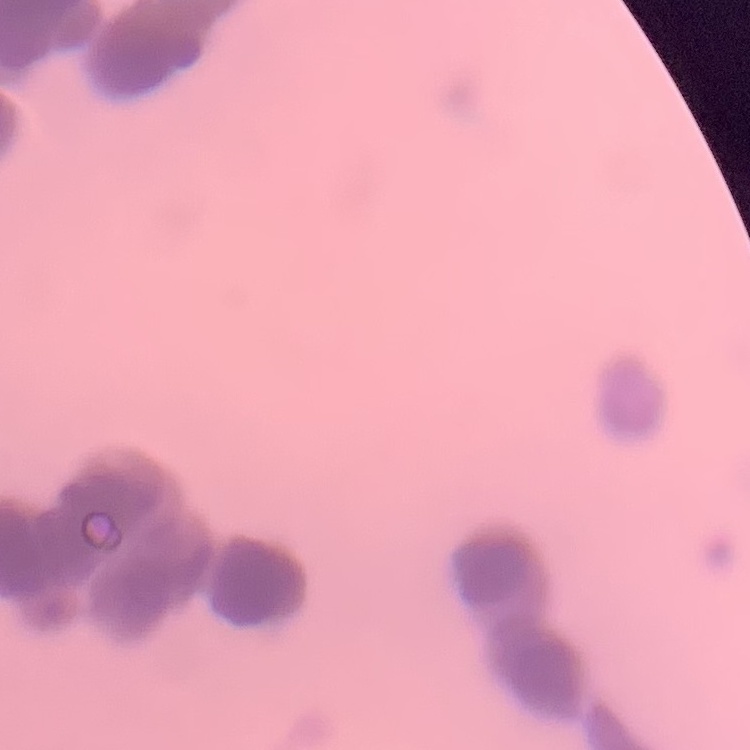
The red blood cells exhibit rouleaux formation. Square crop of a larger photomicrograph. Thin blood film. Field's or Giemsa stain.